Assess this cell for malaria.
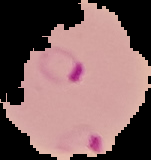
Parasitized.

preparation: thin blood smear
image_size: 151×160 pixels
image_type: segmented cell region on a black background